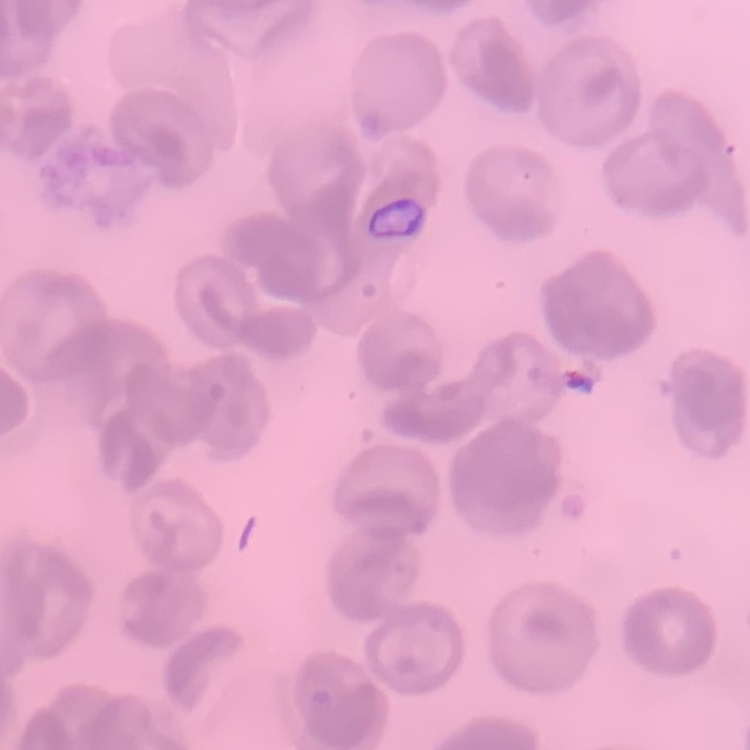
erythrocyte morphology = no rouleaux formation
stain = Field's or Giemsa
preparation = thin peripheral smear
image type = square crop of a larger photomicrograph